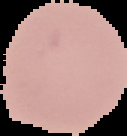

Summary:
  - Image size: 127×136 pixels
  - Result: no Plasmodium parasites detected
  - Image type: segmented cell region with the area outside set to black
  - Preparation: thin blood film